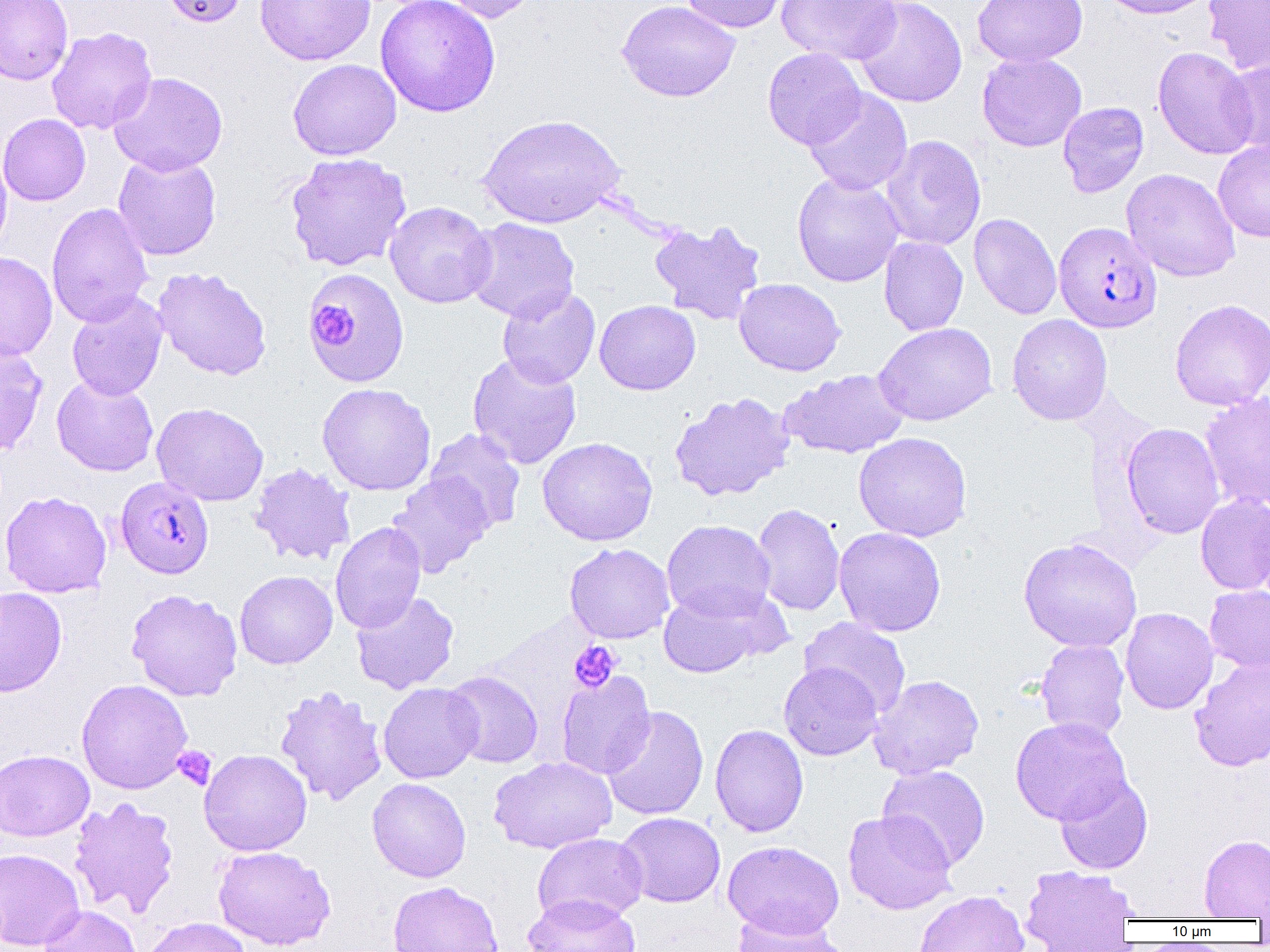

slide-level diagnosis = Plasmodium falciparum
field of view = one of a larger specimen
preparation = thin blood smear
modality = optical microscopy
Plasmodium falciparum-infected red blood cell locations = approximate bounding boxes as named x1/y1/x2/y2 corners in pixels: (x1=1054, y1=222, x2=1161, y2=333), (x1=116, y1=476, x2=214, y2=579)
image size = 1270×952 pixels
uninfected red blood cell locations = approximate bounding boxes as named x1/y1/x2/y2 corners in pixels: (x1=0, y1=0, x2=73, y2=85), (x1=162, y1=0, x2=249, y2=27), (x1=256, y1=0, x2=375, y2=66), (x1=375, y1=0, x2=501, y2=117), (x1=435, y1=0, x2=543, y2=24), (x1=678, y1=0, x2=791, y2=33), (x1=777, y1=0, x2=902, y2=65), (x1=854, y1=0, x2=967, y2=107), (x1=972, y1=0, x2=1088, y2=67), (x1=1095, y1=0, x2=1218, y2=19), (x1=1202, y1=0, x2=1270, y2=75), (x1=617, y1=1, x2=740, y2=102), (x1=46, y1=26, x2=157, y2=135), (x1=1152, y1=46, x2=1259, y2=160), (x1=763, y1=47, x2=866, y2=150), (x1=977, y1=51, x2=1087, y2=152), (x1=1220, y1=56, x2=1270, y2=159), (x1=288, y1=59, x2=401, y2=160), (x1=109, y1=72, x2=228, y2=175), (x1=804, y1=89, x2=913, y2=195), (x1=1058, y1=102, x2=1149, y2=198), (x1=0, y1=114, x2=91, y2=206), (x1=477, y1=114, x2=625, y2=229), (x1=879, y1=135, x2=987, y2=251), (x1=1213, y1=137, x2=1270, y2=243), (x1=0, y1=146, x2=12, y2=259), (x1=285, y1=152, x2=412, y2=272), (x1=113, y1=153, x2=221, y2=261), (x1=1121, y1=168, x2=1241, y2=282), (x1=792, y1=173, x2=904, y2=287), (x1=385, y1=201, x2=496, y2=308), (x1=46, y1=203, x2=154, y2=328), (x1=969, y1=213, x2=1062, y2=320), (x1=463, y1=218, x2=580, y2=323), (x1=648, y1=218, x2=767, y2=325), (x1=879, y1=236, x2=968, y2=336), (x1=0, y1=251, x2=57, y2=362), (x1=152, y1=267, x2=272, y2=380), (x1=303, y1=268, x2=411, y2=387), (x1=734, y1=278, x2=846, y2=376), (x1=497, y1=287, x2=601, y2=389), (x1=66, y1=291, x2=168, y2=401), (x1=1169, y1=299, x2=1270, y2=410), (x1=595, y1=300, x2=701, y2=395), (x1=1007, y1=314, x2=1112, y2=425), (x1=873, y1=322, x2=997, y2=426), (x1=0, y1=340, x2=48, y2=457), (x1=467, y1=353, x2=582, y2=470), (x1=780, y1=368, x2=909, y2=459), (x1=51, y1=375, x2=159, y2=476), (x1=317, y1=383, x2=436, y2=496), (x1=1200, y1=391, x2=1270, y2=512), (x1=669, y1=392, x2=795, y2=502), (x1=151, y1=402, x2=268, y2=506), (x1=1121, y1=423, x2=1225, y2=539), (x1=425, y1=428, x2=526, y2=533), (x1=853, y1=432, x2=972, y2=542), (x1=537, y1=437, x2=658, y2=546), (x1=249, y1=463, x2=357, y2=566), (x1=387, y1=474, x2=493, y2=577), (x1=0, y1=491, x2=112, y2=598), (x1=1195, y1=494, x2=1270, y2=594), (x1=1251, y1=500, x2=1270, y2=606), (x1=752, y1=503, x2=845, y2=617), (x1=661, y1=519, x2=776, y2=621), (x1=330, y1=522, x2=426, y2=633), (x1=834, y1=527, x2=946, y2=637), (x1=1018, y1=537, x2=1143, y2=652), (x1=564, y1=542, x2=675, y2=644), (x1=234, y1=570, x2=338, y2=668), (x1=1205, y1=585, x2=1270, y2=674), (x1=0, y1=586, x2=67, y2=697), (x1=657, y1=586, x2=781, y2=678), (x1=126, y1=588, x2=243, y2=702), (x1=351, y1=591, x2=459, y2=694), (x1=1120, y1=607, x2=1218, y2=714), (x1=799, y1=617, x2=912, y2=718), (x1=1035, y1=639, x2=1130, y2=741), (x1=1189, y1=657, x2=1270, y2=771), (x1=779, y1=662, x2=883, y2=761), (x1=556, y1=670, x2=656, y2=779), (x1=442, y1=671, x2=544, y2=768), (x1=869, y1=674, x2=984, y2=780), (x1=76, y1=679, x2=193, y2=794), (x1=378, y1=682, x2=483, y2=783), (x1=274, y1=685, x2=388, y2=806), (x1=601, y1=705, x2=709, y2=821), (x1=1010, y1=717, x2=1131, y2=825), (x1=709, y1=724, x2=809, y2=837), (x1=0, y1=749, x2=94, y2=841), (x1=199, y1=749, x2=312, y2=856), (x1=488, y1=756, x2=617, y2=854), (x1=877, y1=765, x2=991, y2=870), (x1=1054, y1=774, x2=1153, y2=874), (x1=367, y1=777, x2=471, y2=883), (x1=68, y1=797, x2=180, y2=920), (x1=843, y1=809, x2=957, y2=915), (x1=615, y1=812, x2=726, y2=907), (x1=532, y1=833, x2=647, y2=925), (x1=1199, y1=834, x2=1270, y2=919), (x1=723, y1=840, x2=844, y2=939), (x1=213, y1=845, x2=336, y2=950), (x1=0, y1=848, x2=85, y2=951), (x1=1020, y1=864, x2=1140, y2=950), (x1=387, y1=881, x2=503, y2=952), (x1=913, y1=889, x2=1029, y2=952), (x1=522, y1=892, x2=641, y2=952), (x1=38, y1=904, x2=142, y2=952), (x1=729, y1=910, x2=849, y2=952), (x1=141, y1=917, x2=253, y2=952)
magnification = 1000x
platelet locations = approximate bounding boxes as named x1/y1/x2/y2 corners in pixels: (x1=310, y1=305, x2=351, y2=344), (x1=569, y1=641, x2=621, y2=693), (x1=172, y1=746, x2=217, y2=790)